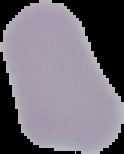
{
  "image_size": "124×154 pixels",
  "malaria_status": "uninfected",
  "image_type": "segmented cell region on a black background",
  "preparation": "thin blood film"
}